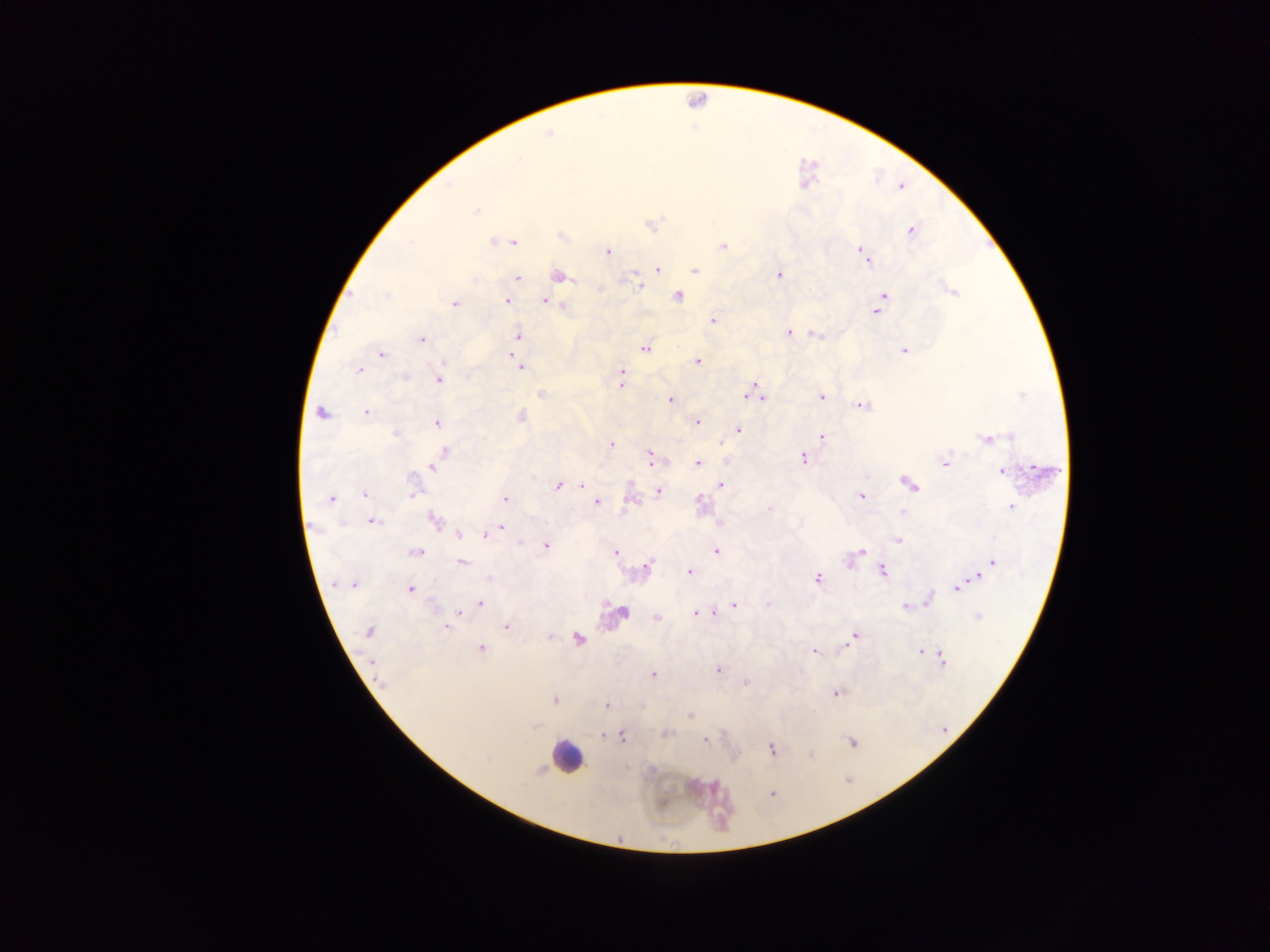 Approximate centers as (x, y) in pixels. Leukocyte locations: (566, 756). Plasmodium parasite locations: (549, 133), (476, 211), (649, 224), (911, 230), (560, 235), (496, 241), (506, 241), (512, 241), (723, 246), (607, 251), (864, 254), (866, 259), (657, 269), (694, 270), (779, 274), (557, 275), (517, 277), (638, 286), (599, 289), (951, 290), (884, 295), (677, 296), (507, 300), (544, 300), (454, 304), (876, 311), (712, 321), (788, 332), (518, 334), (816, 334), (422, 339), (645, 347), (904, 350), (513, 352), (380, 354), (697, 361), (520, 367), (359, 369), (621, 374), (438, 379), (620, 384), (753, 392), (541, 393), (821, 396), (761, 398), (670, 399), (863, 405), (320, 412), (366, 412), (520, 416), (437, 422), (696, 422), (737, 430), (395, 433), (822, 436), (987, 439), (611, 444), (443, 451), (649, 456), (438, 457), (803, 458), (945, 462), (697, 463), (432, 466), (1003, 470), (909, 483), (558, 486), (582, 486), (720, 486), (657, 491), (412, 492), (364, 495), (861, 495), (330, 498), (504, 499), (630, 499), (596, 502), (700, 504), (1011, 506), (899, 513), (372, 520), (433, 520), (500, 528), (458, 533), (485, 534), (897, 541), (521, 542), (545, 545), (715, 550), (614, 551), (415, 552), (860, 552), (856, 554), (850, 560), (461, 562), (992, 562), (646, 567), (882, 571), (689, 572), (978, 577), (489, 578), (817, 578), (336, 583), (353, 584), (956, 588), (410, 589), (929, 597), (479, 603), (734, 605), (768, 605), (905, 607), (458, 613), (621, 613), (694, 613), (655, 617), (979, 617), (506, 627), (447, 628), (368, 631), (550, 637), (577, 638), (853, 638), (480, 648), (814, 651), (920, 651), (941, 658), (718, 669), (653, 674), (380, 683), (745, 684), (836, 692), (555, 700), (606, 705), (690, 715), (664, 733), (621, 736), (703, 740), (852, 741), (772, 748), (811, 755), (772, 793). Sample from Ghana. One field of view. Thick blood smear. Photographed through a microscope with a mobile-phone camera. Image is 1270×952 pixels.